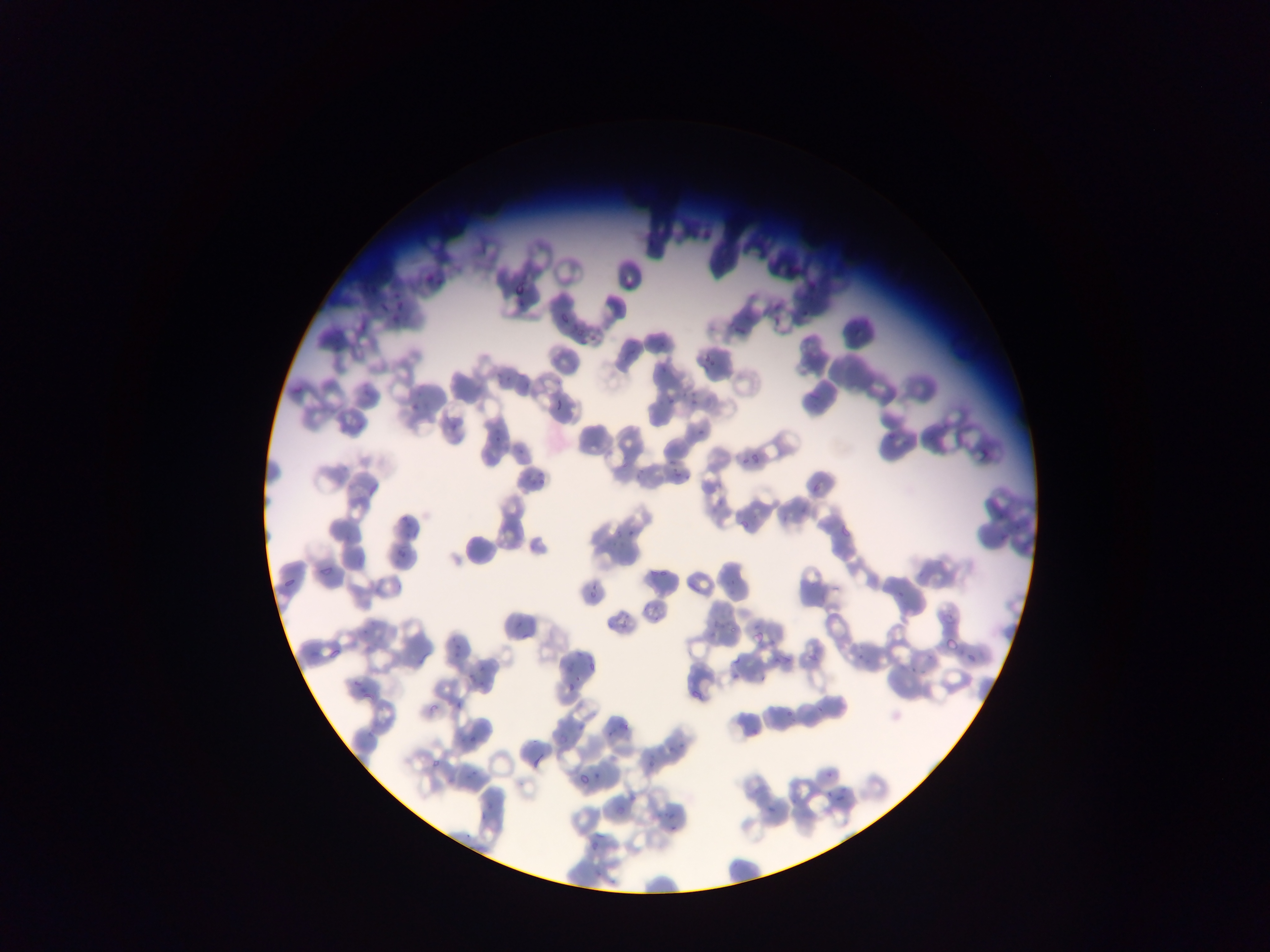

Approximate bounding boxes as {left, top, right, bottom} in pixels.
Summary:
  - Malaria parasite locations: {423, 275, 438, 286}, {514, 280, 529, 297}, {393, 295, 405, 315}, {374, 308, 390, 320}, {552, 308, 571, 329}, {768, 311, 784, 327}, {390, 312, 405, 326}, {588, 326, 599, 344}, {732, 326, 748, 338}, {700, 349, 720, 370}, {685, 386, 700, 407}, {553, 395, 563, 414}, {663, 395, 675, 405}, {406, 399, 417, 415}, {691, 420, 709, 438}, {445, 423, 456, 432}, {492, 431, 504, 448}, {516, 444, 528, 458}, {739, 450, 763, 466}, {663, 455, 677, 478}, {673, 467, 686, 483}, {809, 484, 819, 496}, {796, 496, 809, 515}, {398, 514, 408, 526}, {615, 525, 641, 540}, {838, 527, 851, 540}, {395, 545, 407, 560}, {648, 563, 664, 583}, {312, 564, 334, 574}, {279, 575, 300, 589}, {584, 580, 603, 602}, {892, 590, 908, 600}, {705, 607, 724, 632}, {517, 623, 527, 638}, {753, 629, 763, 641}, {450, 636, 465, 658}, {852, 648, 864, 662}, {963, 648, 977, 663}, {721, 651, 738, 683}, {770, 652, 796, 667}, {906, 655, 925, 674}, {567, 664, 577, 674}, {466, 668, 480, 688}, {750, 673, 772, 685}, {563, 674, 579, 694}, {349, 677, 367, 695}, {814, 694, 824, 715}, {781, 703, 795, 719}, {571, 715, 586, 735}, {605, 725, 616, 739}, {558, 733, 568, 740}, {670, 740, 686, 756}, {532, 747, 550, 768}, {647, 755, 657, 774}, {592, 761, 606, 778}, {824, 769, 834, 779}, {575, 773, 591, 787}, {624, 784, 638, 802}, {824, 789, 834, 800}, {834, 794, 844, 810}, {480, 801, 495, 823}, {762, 801, 777, 817}, {655, 803, 668, 818}, {667, 820, 678, 842}, {585, 839, 602, 854}, {590, 874, 609, 887}
  - Capture: mobile-phone photograph through a microscope
  - Image size: 1270×952 pixels
  - Field of view: single
  - Preparation: thin blood film
  - Country: Ghana